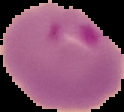

Summary:
  - Preparation: thin blood smear
  - Image size: 124×112 pixels
  - Result: malaria parasites identified
  - Image type: segmented cell region with the area outside set to black